Assess this cell for malaria.
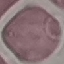
It is uninfected.

Summary:
  - Preparation: thin blood film
  - Stain: Giemsa
  - Capture: smartphone through the microscope eyepiece
  - Image type: automatically extracted cell patch, resized to 64 × 64 pixels